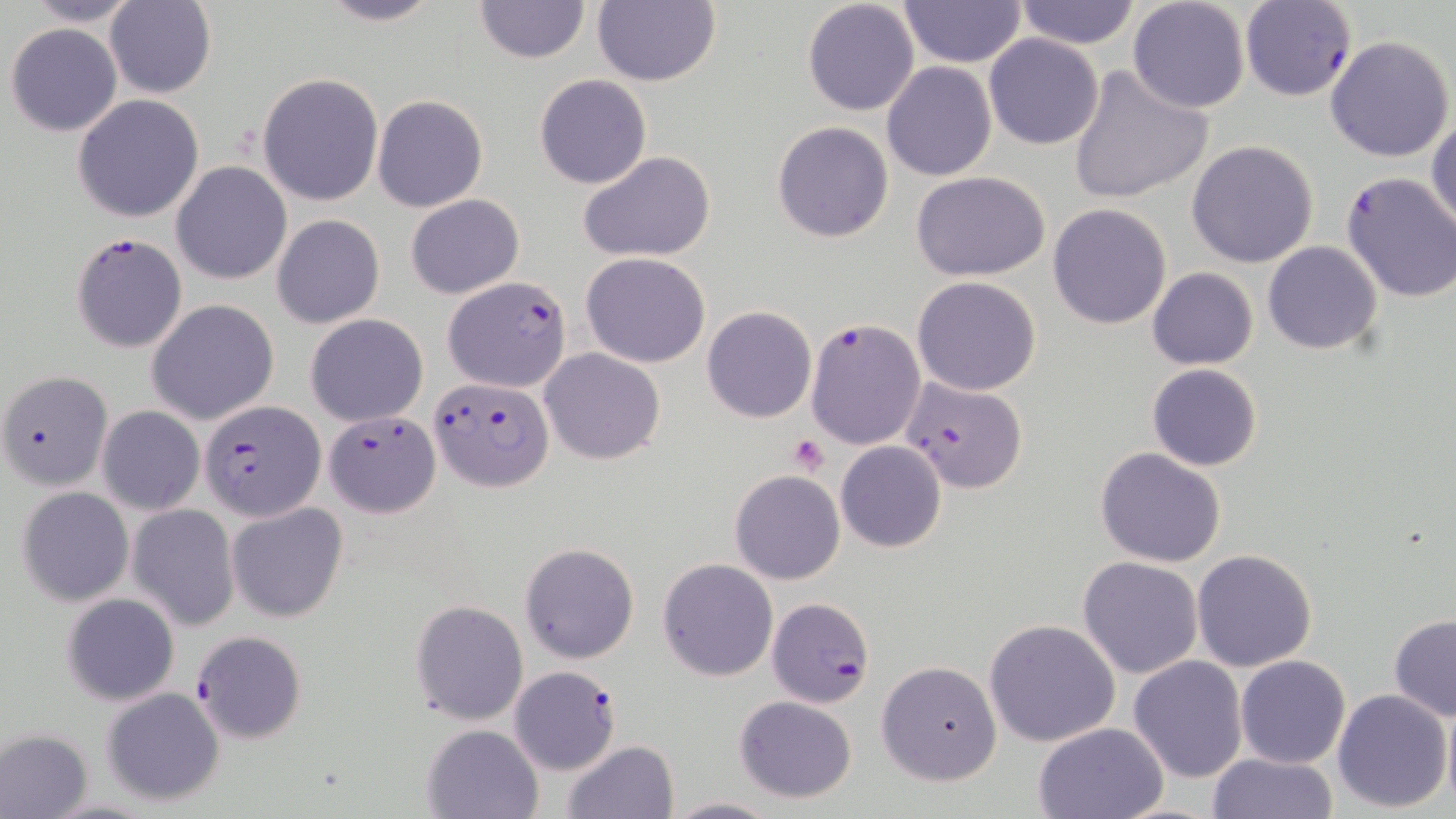

Summary:
  - Coordinate format: approximate bounding boxes as (x1, y1, x2, y2) in pixels
  - Plasmodium falciparum-infected red blood cell locations: (1240, 1, 1359, 102), (70, 232, 188, 354), (443, 273, 573, 391), (807, 317, 923, 448), (429, 375, 554, 492), (901, 375, 1028, 494), (201, 399, 326, 521), (324, 410, 440, 516), (767, 597, 873, 706), (191, 630, 306, 744), (510, 665, 621, 776)
  - Platelet locations: (787, 434, 829, 475)
  - Uninfected red blood cell locations: (21, 0, 145, 26), (312, 0, 444, 26), (475, 0, 588, 64), (592, 0, 720, 88), (898, 0, 1025, 67), (1012, 0, 1139, 48), (104, 1, 216, 99), (802, 1, 920, 117), (1127, 1, 1251, 114), (6, 22, 122, 137), (1326, 34, 1454, 161), (984, 35, 1104, 150), (882, 61, 998, 183), (1067, 62, 1212, 206), (257, 72, 384, 207), (533, 74, 652, 189), (73, 94, 204, 223), (373, 94, 488, 212), (1427, 113, 1456, 239), (771, 120, 894, 243), (1187, 140, 1318, 267), (578, 151, 717, 261), (172, 162, 290, 285), (911, 170, 1051, 281), (1337, 170, 1456, 305), (405, 194, 524, 298), (1048, 202, 1171, 329), (272, 214, 385, 329), (1262, 241, 1383, 354), (581, 253, 712, 368), (1148, 267, 1258, 368), (912, 276, 1041, 395), (147, 298, 279, 425), (702, 306, 816, 424), (305, 313, 429, 425), (540, 348, 665, 464), (1147, 363, 1262, 471), (0, 370, 112, 491), (97, 406, 204, 515), (835, 441, 947, 552), (1095, 446, 1227, 567), (729, 469, 846, 585), (17, 485, 133, 607), (228, 502, 347, 623), (127, 505, 240, 631), (518, 542, 639, 665), (1192, 548, 1318, 672), (1078, 556, 1203, 678), (657, 557, 779, 681), (62, 592, 180, 706), (410, 599, 528, 724), (1388, 615, 1456, 721), (983, 618, 1121, 748), (1128, 656, 1248, 783), (1235, 656, 1351, 769), (877, 660, 1003, 785), (101, 688, 224, 806), (1332, 689, 1452, 811), (733, 696, 858, 804), (1441, 698, 1456, 815), (1033, 721, 1172, 818), (422, 722, 545, 818), (1, 729, 91, 818), (561, 740, 679, 819), (1206, 753, 1337, 819), (667, 794, 775, 818)
  - Slide-level diagnosis: Plasmodium falciparum
  - Stain: May-Grünwald-Giemsa
  - Image size: 1456×819 pixels
  - Magnification: 1000x
  - Modality: light microscopy
  - Preparation: thin blood smear
  - Field of view: single